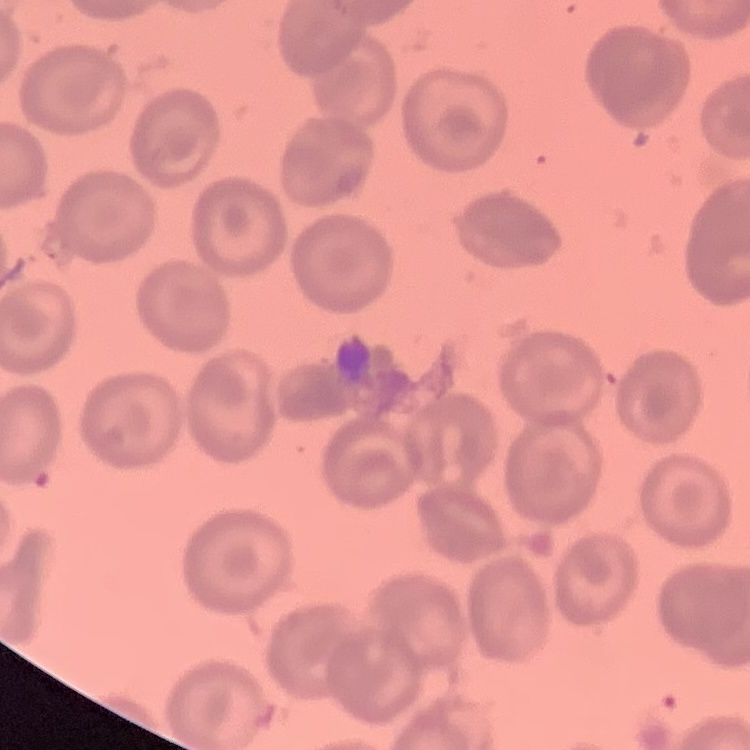 The red blood cells exhibit no rouleaux formation. Field's or Giemsa stain. Thin peripheral smear. One tile cut from a larger photomicrograph.